Identify the blood parasite species.
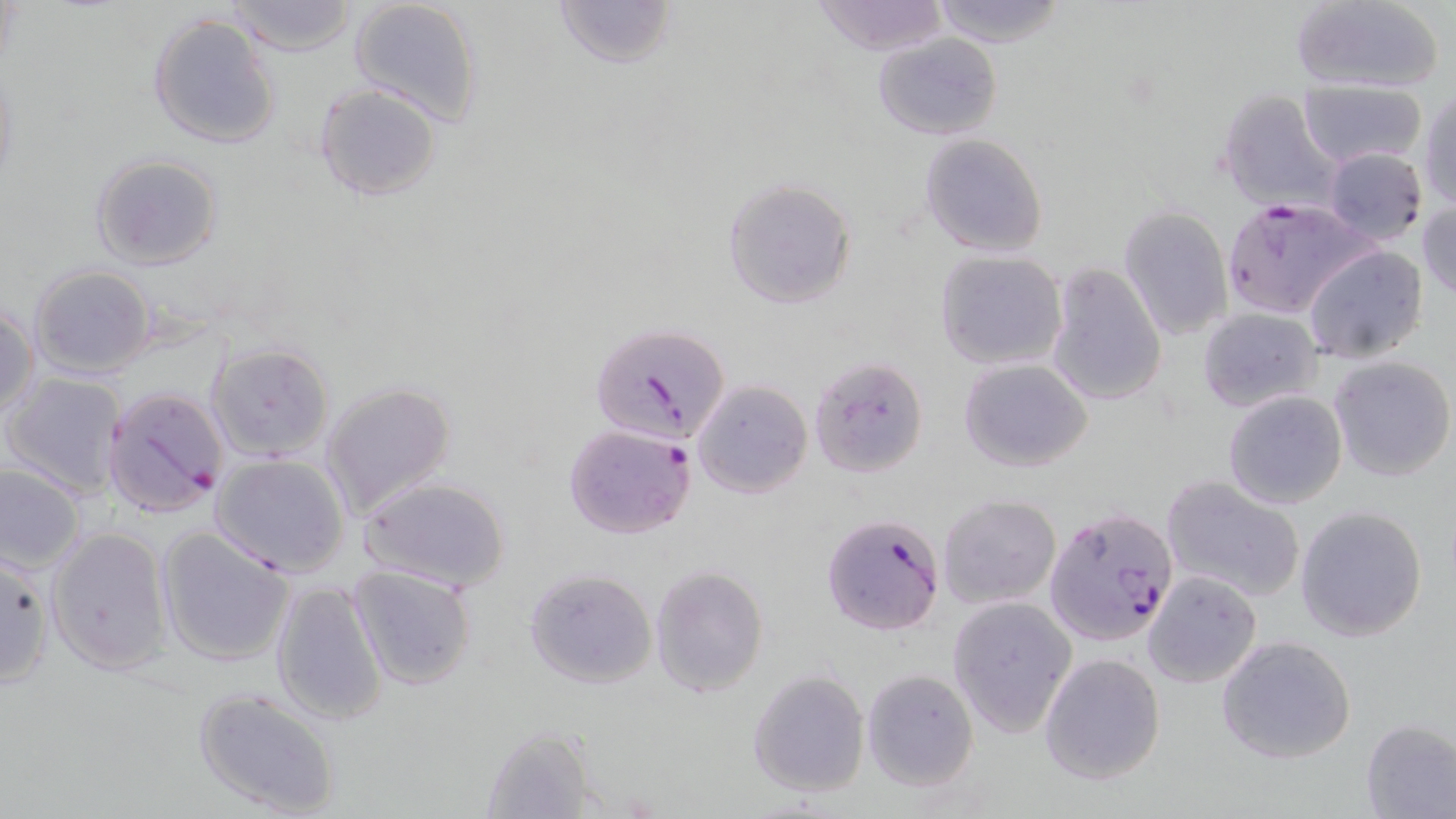

Plasmodium falciparum.

Approximate bounding boxes as named x1/y1/x2/y2 corners in pixels. Plasmodium falciparum-infected red blood cell locations: (x1=1223, y1=200, x2=1369, y2=318), (x1=591, y1=321, x2=730, y2=446), (x1=103, y1=386, x2=230, y2=518), (x1=562, y1=422, x2=696, y2=538), (x1=1046, y1=506, x2=1177, y2=647), (x1=821, y1=514, x2=944, y2=636). Uninfected red blood cell locations: (x1=348, y1=0, x2=484, y2=126), (x1=553, y1=0, x2=678, y2=69), (x1=813, y1=0, x2=950, y2=54), (x1=930, y1=0, x2=1064, y2=47), (x1=1289, y1=0, x2=1448, y2=93), (x1=221, y1=1, x2=357, y2=55), (x1=147, y1=13, x2=282, y2=150), (x1=871, y1=34, x2=1002, y2=142), (x1=1300, y1=79, x2=1425, y2=170), (x1=314, y1=83, x2=442, y2=201), (x1=1216, y1=88, x2=1340, y2=213), (x1=1419, y1=88, x2=1456, y2=210), (x1=918, y1=134, x2=1048, y2=258), (x1=1322, y1=147, x2=1428, y2=244), (x1=90, y1=154, x2=223, y2=271), (x1=722, y1=177, x2=856, y2=309), (x1=1418, y1=199, x2=1456, y2=301), (x1=1119, y1=206, x2=1233, y2=341), (x1=1302, y1=244, x2=1428, y2=363), (x1=935, y1=250, x2=1068, y2=371), (x1=1044, y1=261, x2=1168, y2=408), (x1=29, y1=264, x2=155, y2=378), (x1=0, y1=306, x2=38, y2=421), (x1=1198, y1=307, x2=1323, y2=412), (x1=205, y1=342, x2=334, y2=460), (x1=807, y1=354, x2=928, y2=479), (x1=1328, y1=354, x2=1455, y2=481), (x1=959, y1=357, x2=1094, y2=471), (x1=4, y1=372, x2=127, y2=499), (x1=1224, y1=376, x2=1453, y2=497), (x1=691, y1=379, x2=813, y2=498), (x1=320, y1=380, x2=457, y2=522), (x1=1223, y1=390, x2=1348, y2=510), (x1=212, y1=454, x2=351, y2=577), (x1=0, y1=463, x2=87, y2=573), (x1=357, y1=475, x2=511, y2=593), (x1=1160, y1=477, x2=1307, y2=603), (x1=937, y1=493, x2=1062, y2=610), (x1=1295, y1=505, x2=1428, y2=642), (x1=46, y1=526, x2=170, y2=674), (x1=155, y1=526, x2=296, y2=668), (x1=0, y1=554, x2=55, y2=683), (x1=650, y1=563, x2=769, y2=696), (x1=348, y1=564, x2=479, y2=690), (x1=523, y1=566, x2=657, y2=689), (x1=1141, y1=570, x2=1262, y2=688), (x1=269, y1=578, x2=390, y2=725), (x1=945, y1=595, x2=1078, y2=739), (x1=1215, y1=635, x2=1357, y2=765), (x1=1037, y1=652, x2=1165, y2=785), (x1=747, y1=669, x2=872, y2=797), (x1=861, y1=669, x2=979, y2=791), (x1=193, y1=687, x2=342, y2=818), (x1=1360, y1=718, x2=1456, y2=819), (x1=480, y1=726, x2=600, y2=819). 1000x magnification. Thin blood film. One field of a larger specimen. Image is 1456×819 pixels. Optical microscopy. May-Grünwald-Giemsa-stained preparation.